Assess this cell for malaria.
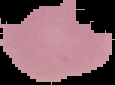
Uninfected.

Summary:
  - Image type: segmented cell region on a black background
  - Image size: 115×85 pixels
  - Preparation: thin blood smear